Locate every Trypanosoma brucei.
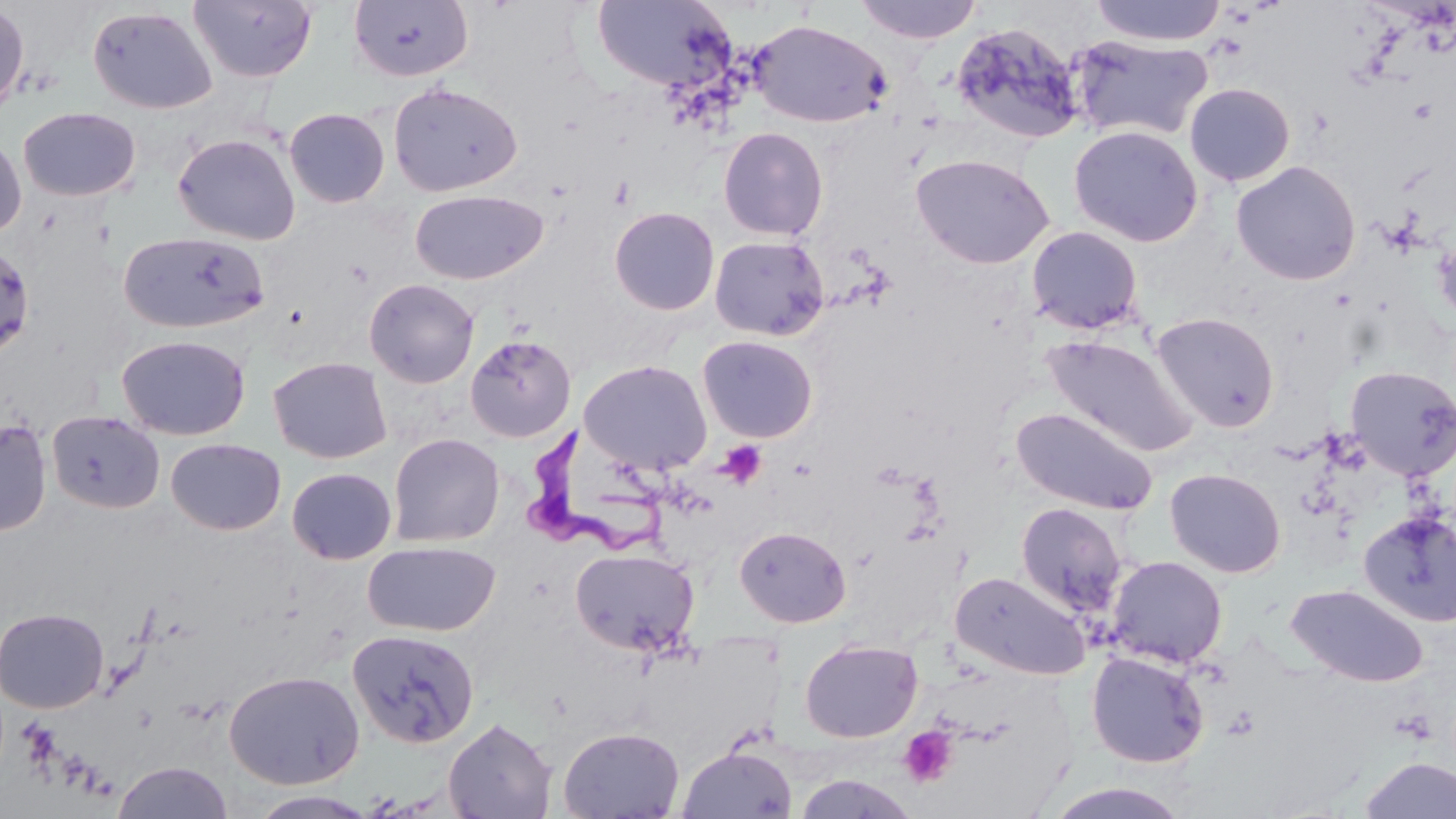

Approximate bounding boxes as (x1, y1, x2, y2) in pixels.
Trypanosoma brucei: (516, 428, 677, 561).

Summary:
  - Uninfected red blood cell locations: (855, 0, 982, 45), (1089, 0, 1227, 47), (188, 1, 318, 83), (348, 1, 474, 83), (592, 1, 737, 93), (0, 2, 30, 118), (87, 6, 218, 114), (749, 19, 892, 128), (950, 21, 1087, 146), (1068, 34, 1214, 143), (387, 81, 523, 197), (1184, 82, 1295, 186), (284, 107, 390, 208), (18, 108, 141, 201), (1068, 124, 1203, 247), (718, 126, 829, 241), (0, 131, 27, 240), (172, 133, 300, 245), (910, 153, 1055, 269), (1230, 160, 1362, 285), (409, 190, 547, 285), (609, 207, 720, 315), (1026, 225, 1144, 335), (119, 231, 269, 334), (708, 234, 830, 341), (1434, 235, 1456, 328), (0, 243, 36, 359), (364, 278, 480, 388), (1151, 312, 1279, 432), (116, 334, 251, 440), (465, 334, 576, 442), (1041, 334, 1198, 458), (697, 335, 818, 443), (268, 357, 392, 464), (580, 360, 712, 475), (1345, 365, 1456, 481), (1011, 406, 1158, 516), (47, 410, 164, 515), (0, 419, 52, 537), (388, 433, 505, 547), (166, 438, 286, 535), (287, 467, 398, 565), (1164, 467, 1286, 578), (1015, 503, 1129, 617), (1358, 509, 1456, 627), (735, 525, 851, 628), (362, 540, 501, 637), (569, 547, 700, 657), (1105, 555, 1228, 669), (950, 570, 1092, 680), (1286, 584, 1429, 687), (0, 607, 109, 713), (346, 628, 480, 748), (799, 638, 923, 743), (1086, 651, 1211, 768), (224, 670, 365, 789), (443, 717, 558, 818), (558, 726, 684, 818), (677, 744, 797, 818), (1358, 756, 1456, 818), (113, 760, 233, 819), (792, 773, 921, 818), (1042, 782, 1196, 818), (247, 789, 381, 818)
  - Platelet locations: (715, 439, 768, 490), (898, 725, 959, 789)
  - Slide-level diagnosis: Trypanosoma brucei
  - Modality: optical microscopy
  - Image size: 1456×819 pixels
  - Preparation: thin blood film
  - Stain: May-Grünwald-Giemsa
  - Magnification: 1000x
  - Field of view: single